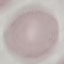

{
  "malaria_status": "uninfected",
  "preparation": "thin blood smear",
  "capture": "smartphone through the microscope eyepiece",
  "image_type": "cell patch, automatically extracted from a larger field of view and resized to 64 × 64 pixels",
  "stain": "Giemsa"
}